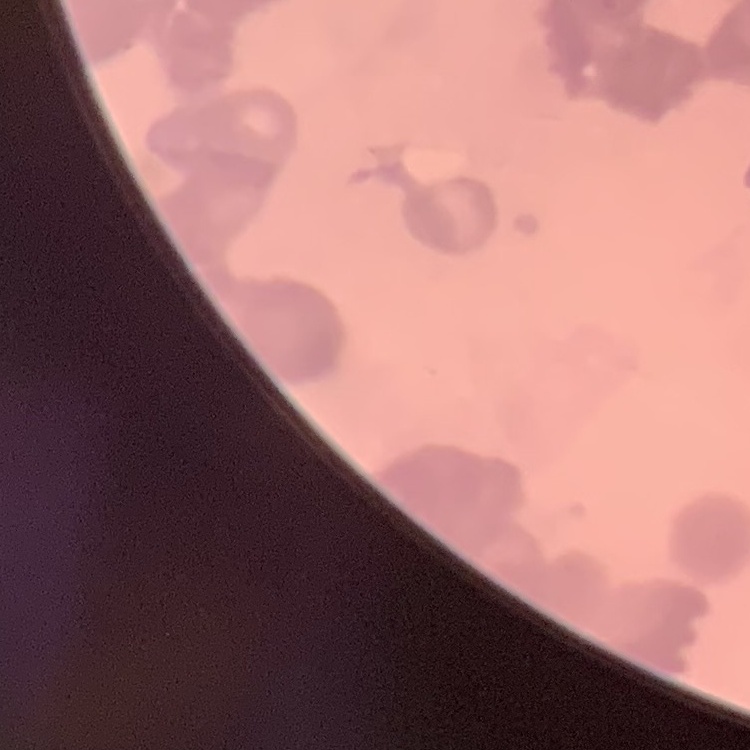

red blood cell morphology = rouleaux formation
image type = one tile cut from a larger photomicrograph
stain = Field's or Giemsa
preparation = thin peripheral smear